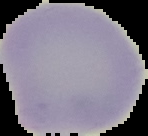

malaria status = uninfected
image size = 148×136 pixels
image type = segmented cell region with the area outside set to black
preparation = thin blood smear